Report the malaria status of this cell.
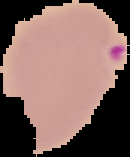

It is parasitized.

Image is 130×157 pixels. Cell region segmented out of the field of view; the surrounding area is masked to black. From a thin blood smear.